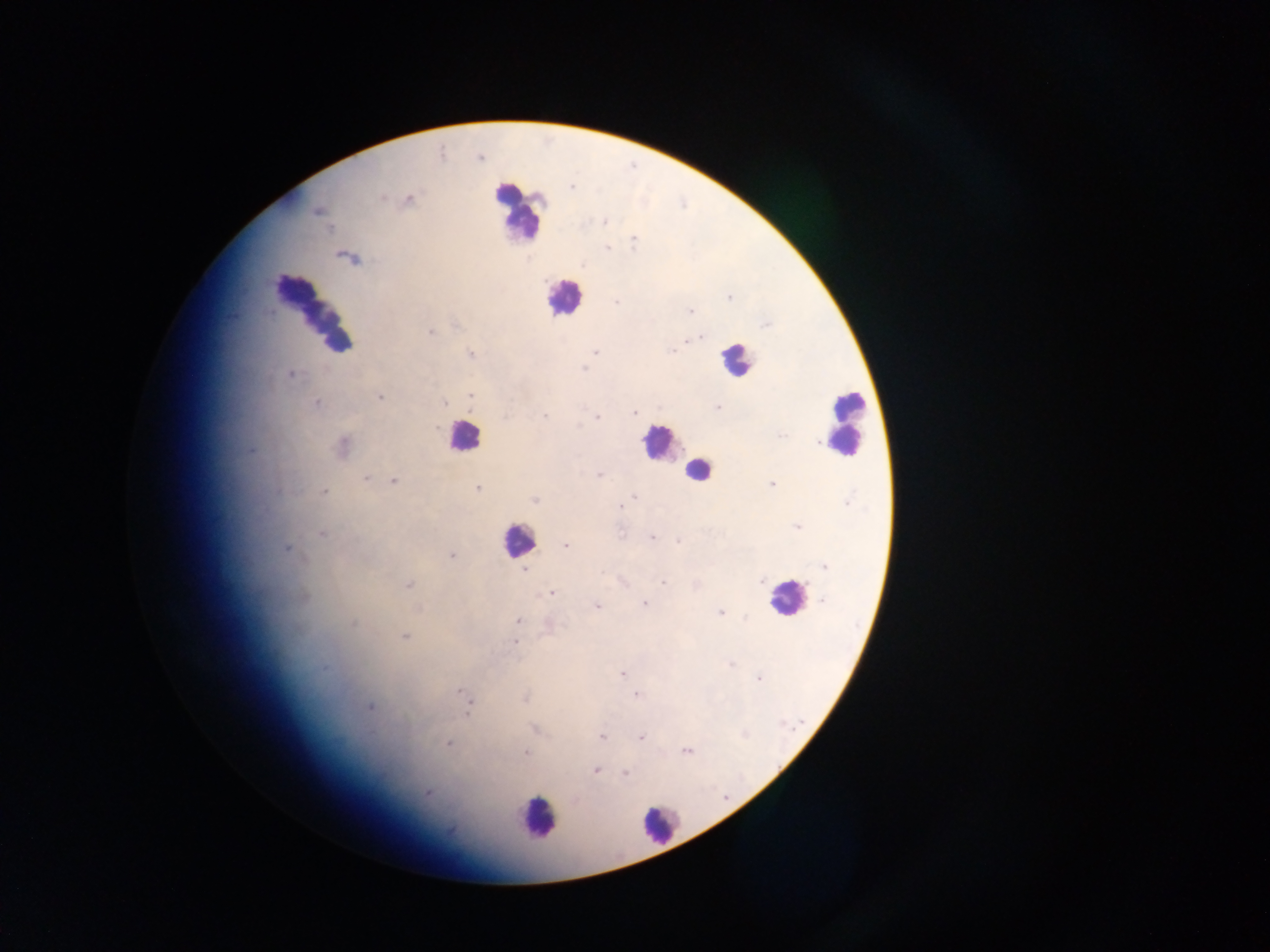
Approximate centers as [x, y] in pixels. Leukocyte locations: [516, 211], [563, 297], [314, 307], [735, 360], [845, 422], [462, 437], [660, 443], [697, 471], [517, 540], [786, 597], [537, 818], [659, 825]. Malaria parasite locations: [480, 158], [382, 198], [409, 199], [317, 211], [604, 222], [634, 241], [607, 248], [729, 298], [616, 302], [691, 311], [430, 332], [699, 338], [672, 350], [596, 352], [471, 355], [584, 368], [291, 374], [470, 396], [380, 397], [317, 403], [445, 403], [717, 407], [634, 413], [544, 415], [597, 418], [436, 428], [343, 446], [598, 476], [366, 478], [394, 481], [772, 484], [477, 488], [324, 492], [634, 497], [535, 500], [619, 507], [321, 533], [621, 533], [652, 537], [678, 541], [566, 546], [286, 548], [451, 555], [824, 566], [525, 570], [601, 572], [762, 581], [663, 582], [409, 585], [551, 593], [822, 600], [645, 603], [597, 606], [720, 612], [518, 620], [353, 624], [405, 637], [514, 642], [324, 668], [622, 674], [759, 679], [460, 691], [636, 695], [525, 698], [369, 706], [468, 713], [535, 729], [602, 737], [641, 737], [448, 743], [686, 751], [525, 753], [595, 770], [626, 773], [427, 794], [575, 800]. Collected in Ghana. Image is 1270×952 pixels. Thick blood film. One field of view. Photographed through a microscope with a mobile-phone camera.